Locate every uninfected red blood cell.
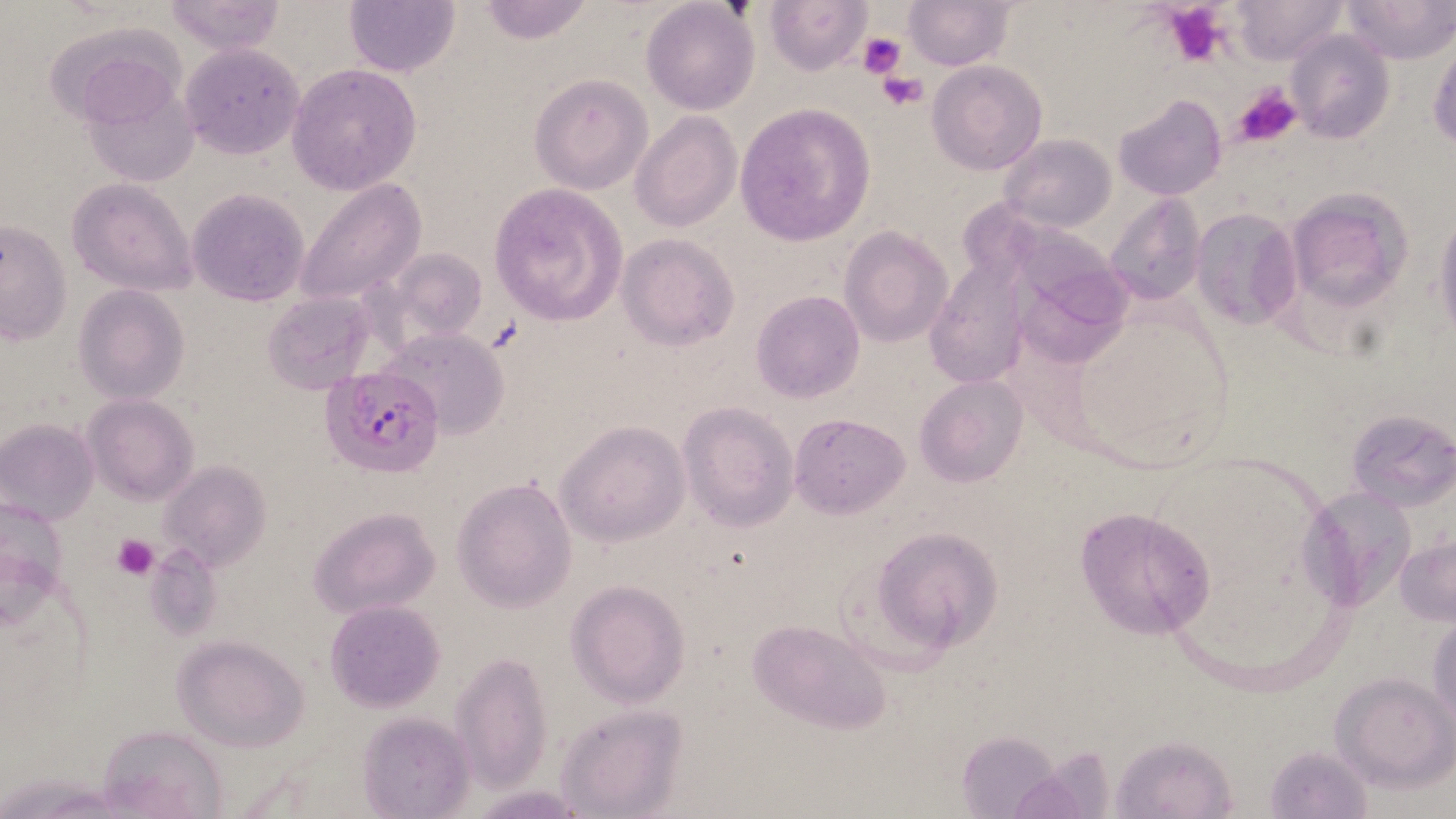

Approximate bounding boxes as [x1, y1, x2, y2] in pixels.
Uninfected red blood cells: [163, 0, 286, 55], [765, 0, 873, 75], [1229, 0, 1346, 64], [1341, 0, 1453, 63], [343, 1, 462, 76], [473, 1, 598, 46], [905, 1, 1011, 71], [640, 2, 759, 115], [1285, 32, 1395, 144], [1428, 36, 1456, 149], [178, 43, 304, 158], [929, 61, 1046, 175], [287, 64, 420, 194], [529, 74, 652, 193], [77, 78, 200, 190], [1115, 93, 1229, 201], [734, 103, 876, 247], [630, 111, 740, 230], [1000, 134, 1116, 233], [67, 178, 197, 296], [294, 178, 427, 309], [489, 183, 626, 326], [1284, 185, 1414, 313], [187, 187, 311, 307], [1103, 194, 1207, 307], [1434, 207, 1456, 351], [1192, 208, 1301, 331], [1, 219, 72, 346], [840, 226, 952, 346], [616, 234, 739, 350], [1011, 236, 1140, 367], [380, 247, 490, 349], [925, 258, 1028, 389], [75, 283, 189, 403], [262, 290, 374, 393], [750, 291, 864, 402], [376, 326, 512, 440], [916, 376, 1028, 487], [83, 395, 197, 504], [678, 402, 798, 532], [1346, 408, 1455, 511], [789, 413, 910, 518], [0, 418, 99, 524], [557, 419, 690, 547], [158, 460, 271, 573], [452, 476, 578, 614], [1301, 481, 1422, 611], [1074, 505, 1219, 640], [308, 506, 442, 620], [868, 526, 1004, 659], [1396, 534, 1456, 627], [565, 579, 691, 707], [326, 600, 445, 713], [1428, 607, 1455, 738], [746, 619, 892, 736], [173, 636, 310, 752], [449, 651, 553, 792], [1332, 672, 1454, 788], [555, 703, 688, 818], [357, 712, 474, 819], [94, 725, 230, 817], [956, 731, 1065, 817], [1111, 734, 1237, 819], [1265, 744, 1372, 817], [469, 785, 588, 816].

slide-level diagnosis = Plasmodium falciparum
preparation = thin blood smear
stain = May-Grünwald-Giemsa
modality = light microscopy
platelet locations = approximate bounding boxes as [x1, y1, x2, y2] in pixels: [1160, 2, 1227, 66], [858, 32, 905, 78], [879, 73, 929, 111], [1233, 83, 1301, 149], [111, 533, 159, 581]
magnification = 1000x
field of view = one of a larger specimen
Plasmodium falciparum-infected red blood cell locations = approximate bounding boxes as [x1, y1, x2, y2] in pixels: [321, 364, 446, 479]
image size = 1456×819 pixels